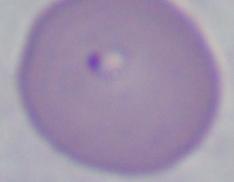

identification: Babesia
modality: micrograph
magnification: 1000x